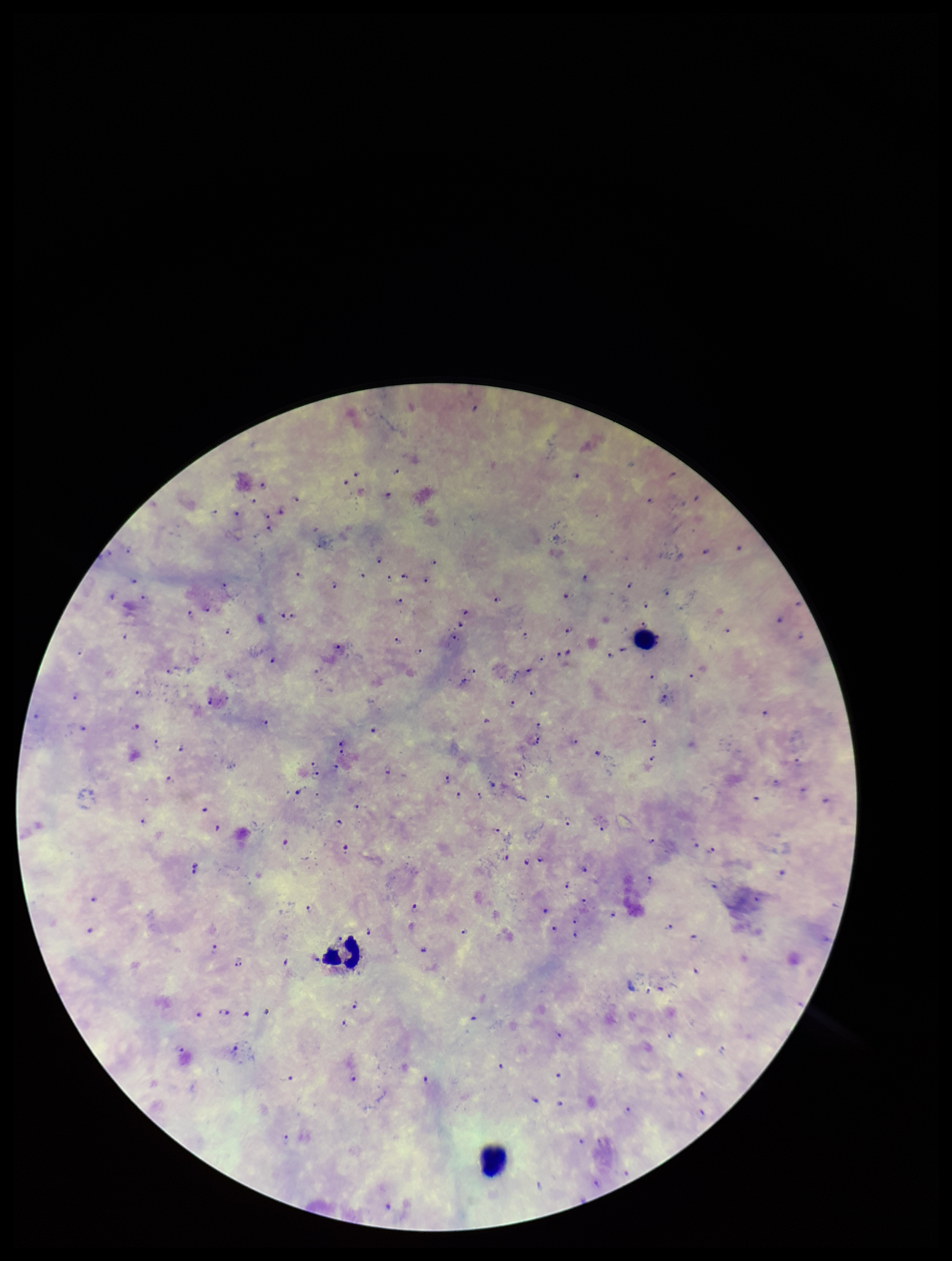
patient malaria status = infected
parasite count = 114
Plasmodium parasites = identified
leukocyte count = 3
image size = 952×1261 pixels
field of view = one from this slide
capture = smartphone photograph through the microscope eyepiece
species reported for this patient = Plasmodium falciparum
stain = Giemsa
preparation = thick smear